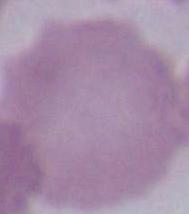 Micrograph. Captured at 1000x magnification. A red blood cell is seen.